Report the malaria status of this cell.
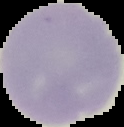
It is uninfected.

image type = segmented cell region with the area outside set to black
image size = 124×127 pixels
preparation = thin blood film